Report the malaria status of this cell.
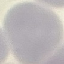

Uninfected.

Cell patch, automatically extracted from a larger field of view and resized to 64 × 64 pixels. Giemsa-stained preparation. Acquired by smartphone through the microscope eyepiece. Thin blood film.